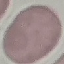
Result: no malaria parasites seen. Giemsa stain. Thin smear of blood. Acquired by smartphone through the microscope eyepiece. Automatically extracted cell patch, resized to 64 × 64 pixels.